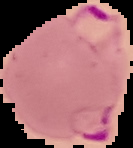 Result: malaria parasites detected. Image is 133×148 pixels. Segmented cell region on a black background. From a thin blood film.